Assess this cell for malaria.
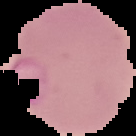
It is parasitized.

image size = 136×136 pixels
preparation = thin blood film
image type = cell region segmented out of the field of view; surrounding area masked to black